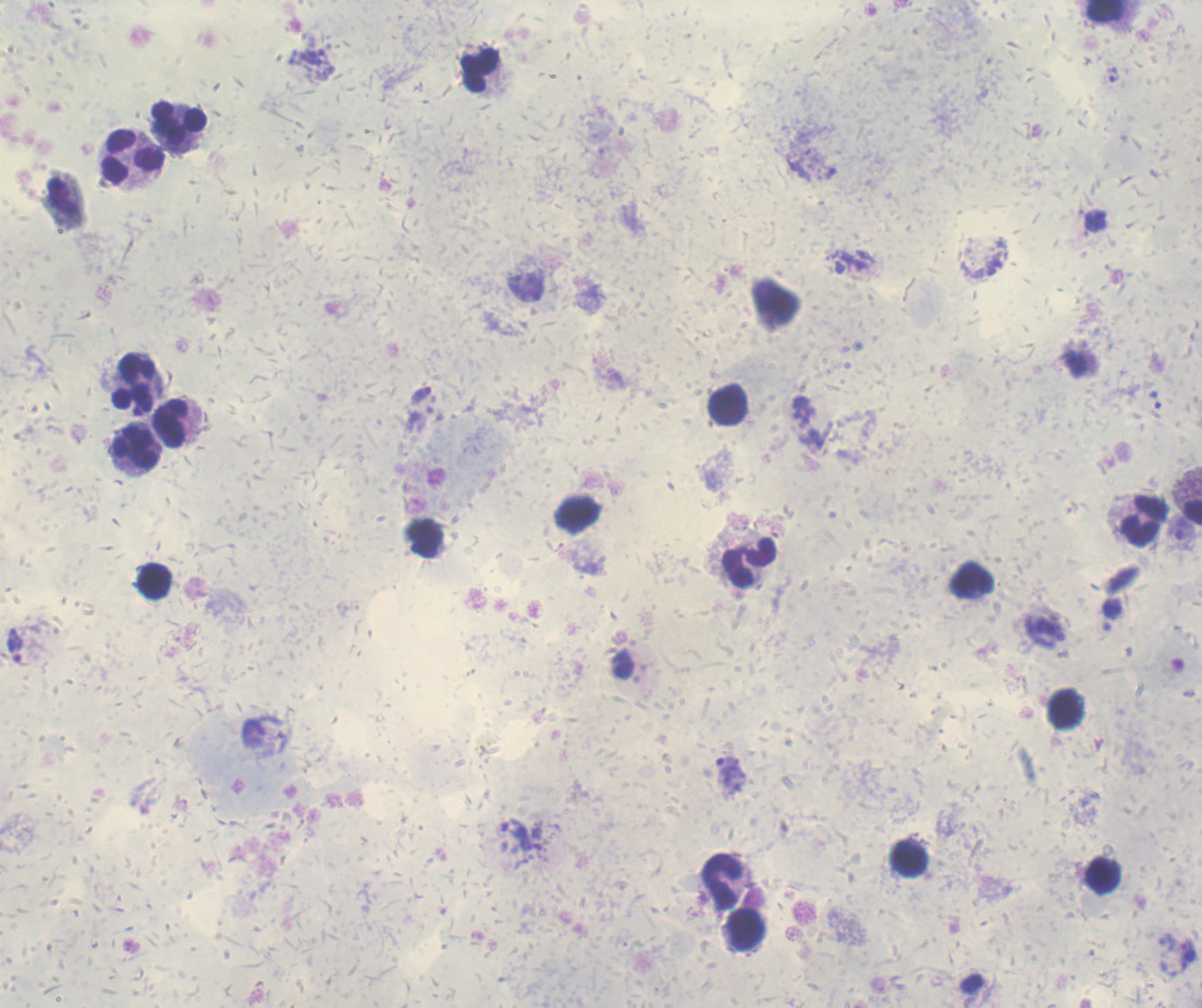

Approximate centers as (x, y) in pixels. Leukocyte locations: (1104, 11), (480, 71), (181, 125), (133, 157), (135, 384), (728, 405), (174, 423), (135, 449), (1192, 512), (576, 515), (1141, 522), (749, 562), (154, 581), (1067, 709), (909, 859), (1102, 876), (722, 881), (744, 929). Trophozoite locations: (1112, 74), (420, 394), (15, 646), (730, 775), (1187, 957). Image is 1202×1008 pixels. One field from this slide. Result: malaria parasites identified. Captured at 100x magnification. Background quality: unsatisfactory. Previously used in a real diagnosis. Coloration quality: good. Romanowsky-stained preparation. Thick blood film.